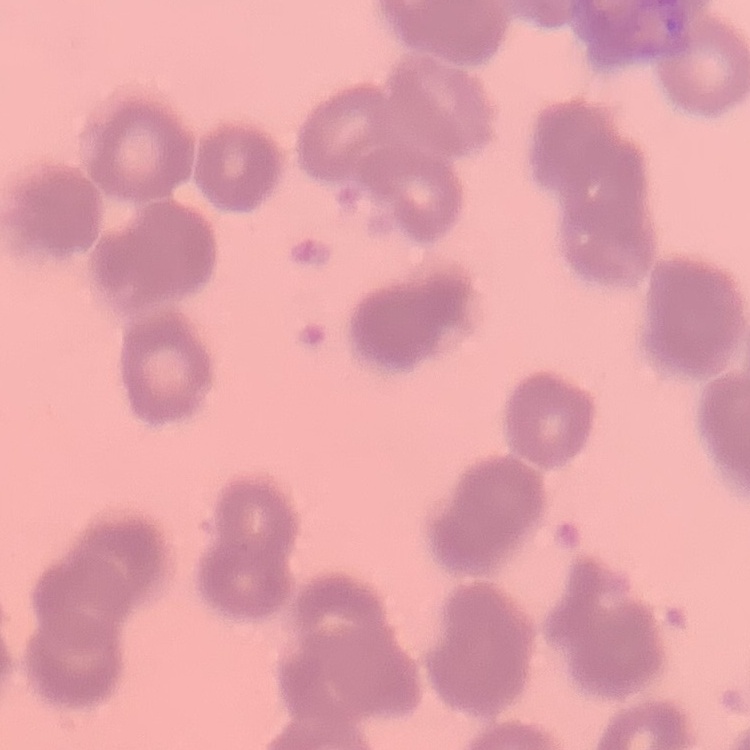

{
  "erythrocyte_morphology": "rouleaux formation",
  "stain": "Field's or Giemsa",
  "preparation": "thin blood film",
  "image_type": "square crop of a larger photomicrograph"
}